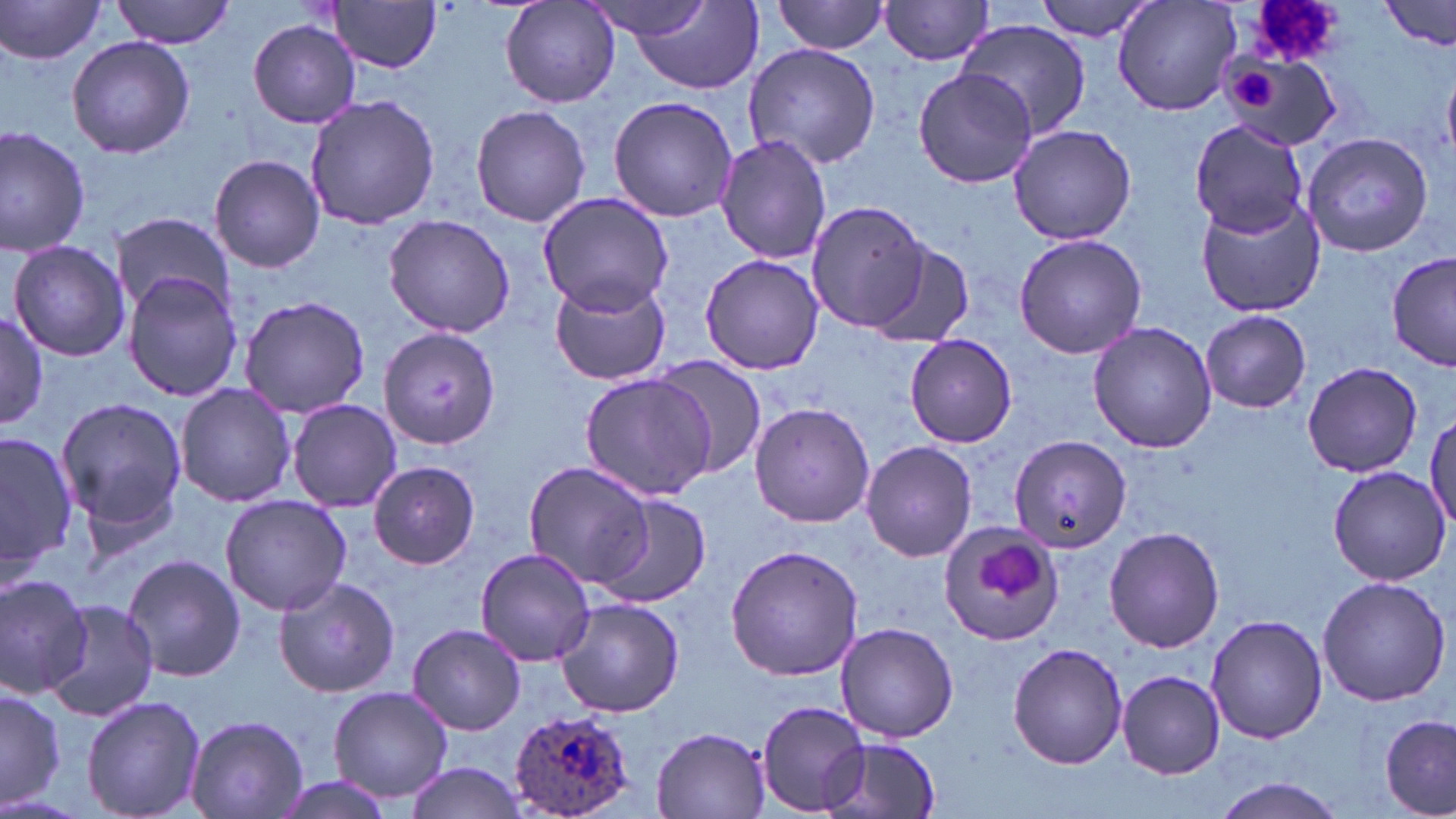
Approximate bounding boxes as [x1, y1, x2, y2] in pixels. Uninfected red blood cell locations: [113, 0, 235, 48], [500, 0, 620, 108], [774, 0, 890, 55], [1036, 0, 1160, 39], [1112, 0, 1243, 117], [1380, 0, 1455, 51], [0, 1, 109, 64], [582, 1, 717, 40], [879, 1, 995, 65], [325, 2, 443, 73], [630, 5, 766, 95], [248, 18, 363, 127], [957, 20, 1093, 141], [67, 35, 194, 160], [743, 43, 882, 170], [1222, 54, 1339, 149], [914, 67, 1037, 191], [1443, 69, 1456, 163], [305, 95, 441, 230], [608, 96, 737, 222], [470, 104, 591, 229], [1190, 119, 1310, 237], [1007, 124, 1137, 245], [0, 125, 91, 256], [1302, 133, 1434, 257], [715, 135, 833, 265], [209, 154, 325, 274], [538, 190, 674, 315], [1197, 198, 1324, 317], [805, 199, 930, 334], [112, 214, 234, 313], [383, 214, 516, 337], [1012, 232, 1147, 358], [7, 240, 131, 361], [862, 241, 975, 350], [1388, 250, 1456, 373], [701, 252, 824, 374], [123, 272, 244, 403], [548, 279, 670, 386], [239, 295, 372, 419], [1200, 310, 1311, 413], [0, 311, 50, 432], [1087, 320, 1219, 452], [378, 327, 502, 447], [904, 335, 1018, 448], [651, 359, 768, 478], [1302, 362, 1423, 478], [578, 371, 719, 501], [176, 383, 296, 508], [55, 397, 188, 534], [286, 398, 404, 513], [748, 402, 876, 528], [1425, 412, 1455, 537], [1, 429, 79, 574], [1010, 435, 1132, 553], [859, 440, 979, 562], [522, 459, 658, 589], [368, 461, 480, 569], [1327, 466, 1451, 585], [220, 494, 352, 616], [593, 496, 711, 608], [939, 520, 1064, 646], [1105, 527, 1227, 653], [725, 544, 864, 681], [475, 545, 593, 666], [124, 554, 246, 682], [0, 571, 95, 698], [1317, 575, 1450, 705], [274, 576, 402, 696], [554, 598, 685, 718], [45, 600, 158, 723], [1207, 613, 1326, 744], [835, 621, 958, 743], [407, 623, 527, 735], [1007, 642, 1128, 769], [1117, 671, 1224, 778], [1, 686, 64, 810], [327, 686, 454, 803], [81, 694, 207, 819], [756, 700, 873, 815], [186, 714, 308, 818], [1380, 715, 1454, 818], [650, 726, 774, 818], [823, 736, 943, 819], [400, 761, 530, 818], [268, 774, 405, 819], [1212, 777, 1347, 818]. Plasmodium ovale-infected red blood cell locations: [510, 707, 638, 819]. Platelet locations: [1219, 63, 1289, 120], [976, 542, 1045, 602]. Slide-level diagnosis: Plasmodium ovale. May-Grünwald-Giemsa stain. Image is 1456×819 pixels. 1000x magnification. Single field of view. Optical microscopy. Thin blood smear.